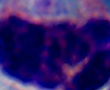 1000x magnification. A leukocyte is seen. Photomicrograph.